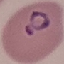
Malaria status: parasitized. Giemsa-stained preparation. Thin blood smear. Photographed with a smartphone camera at the microscope eyepiece. Cell patch, automatically extracted from a larger field of view and resized to 64 × 64 pixels.